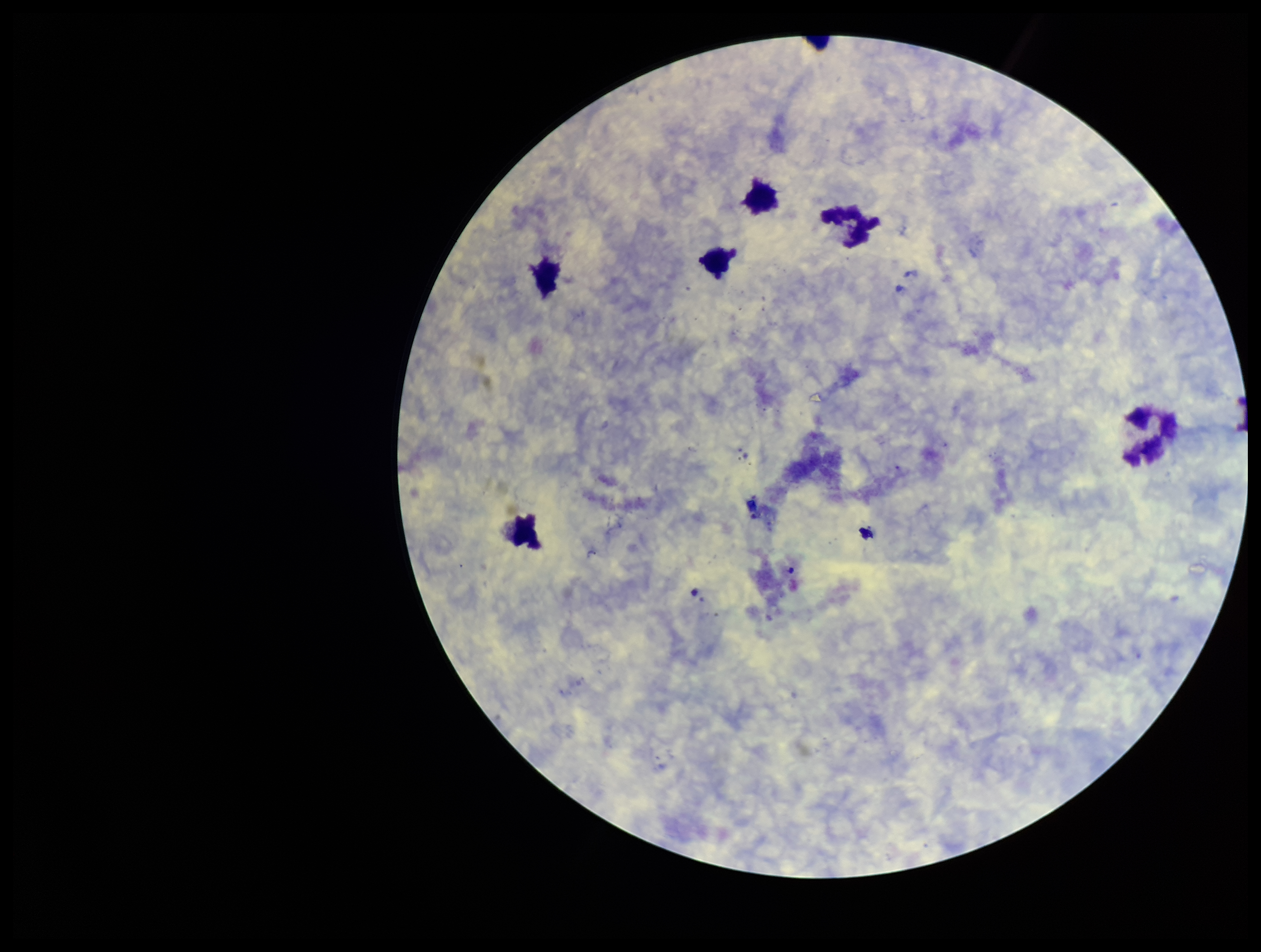
Summary:
  - Field of view: single
  - Parasite count: 0
  - Leukocyte count: 6
  - Capture: smartphone photograph through the microscope eyepiece
  - Preparation: thick
  - Image size: 1261×952 pixels
  - Plasmodium parasites: none identified
  - Stain: Giemsa
  - Patient malaria status: negative